Report the malaria status of this cell.
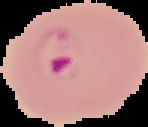
Parasitized.

Summary:
  - Image type: segmented cell region on a black background
  - Image size: 148×127 pixels
  - Preparation: thin blood film